Assess this cell for malaria.
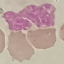
Uninfected.

Automatically extracted cell patch, resized to 64 × 64 pixels. Giemsa stain. Photographed with a smartphone camera at the microscope eyepiece. Thin blood smear.